Report the malaria status of this cell.
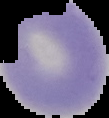
Uninfected.

Summary:
  - Image size: 109×118 pixels
  - Image type: segmented cell region with the area outside set to black
  - Preparation: thin blood film